State which parasite is depicted.
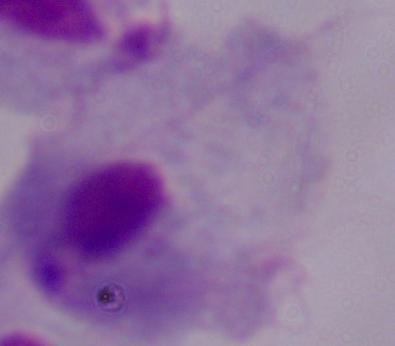
This is a trichomonad.

1000x magnification. Micrograph.